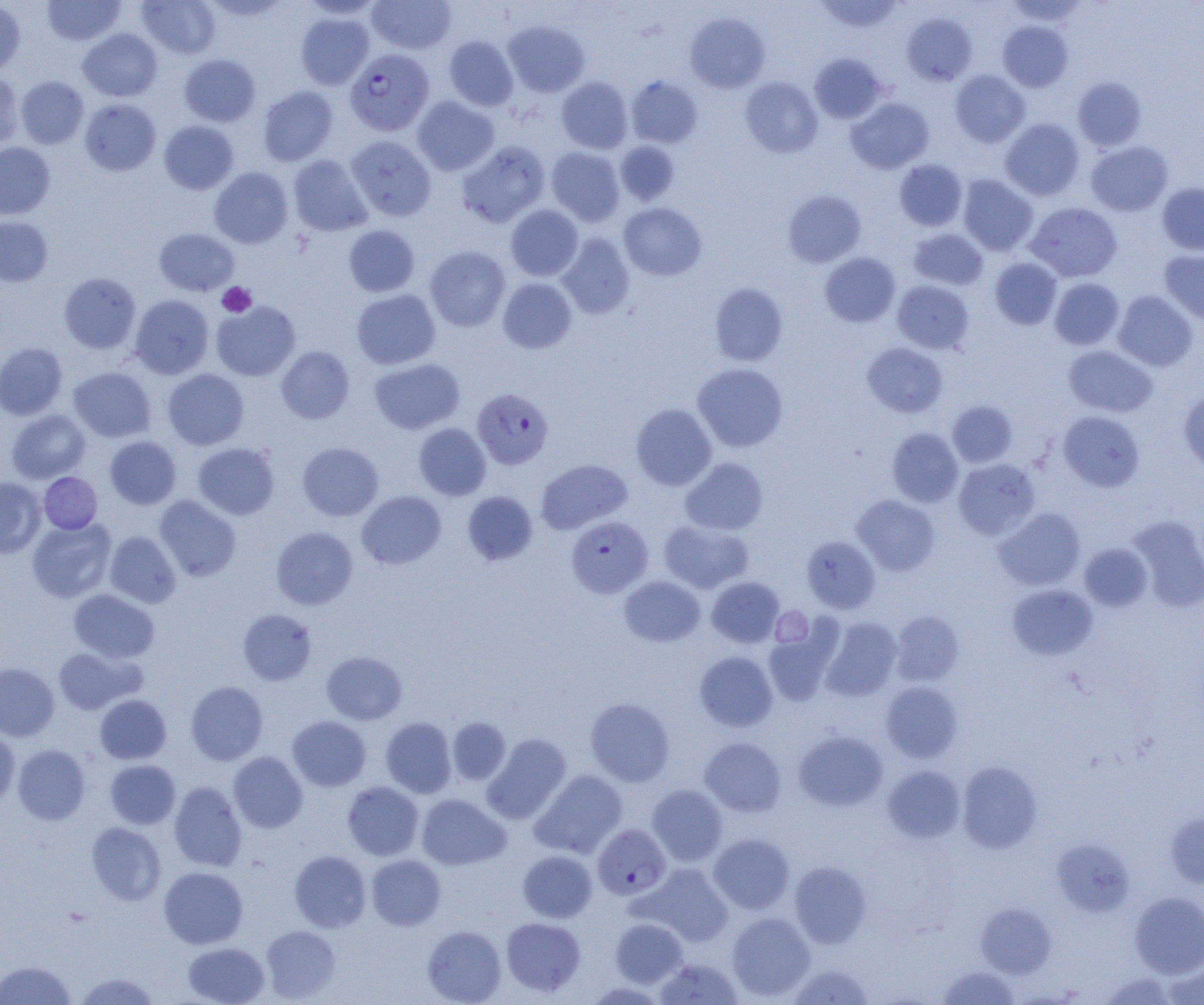
Approximate bounding boxes as [x1, y1, x2, y2] in pixels. Uninfected red blood cell locations: [42, 0, 126, 46], [137, 0, 220, 59], [367, 0, 456, 54], [814, 0, 905, 34], [0, 1, 26, 76], [299, 1, 384, 19], [1004, 1, 1088, 27], [295, 12, 374, 89], [685, 13, 770, 93], [902, 13, 977, 86], [503, 21, 589, 97], [998, 21, 1073, 91], [77, 29, 163, 101], [444, 35, 518, 111], [809, 53, 887, 124], [179, 54, 261, 126], [950, 70, 1030, 147], [0, 72, 23, 151], [626, 75, 703, 148], [16, 76, 89, 149], [556, 77, 633, 153], [740, 77, 823, 158], [1072, 77, 1147, 151], [257, 86, 338, 166], [412, 96, 499, 176], [846, 98, 934, 174], [79, 99, 161, 176], [1000, 118, 1084, 201], [159, 120, 239, 195], [346, 136, 436, 221], [456, 140, 550, 228], [615, 141, 680, 206], [1086, 141, 1174, 216], [0, 142, 55, 220], [546, 147, 625, 226], [288, 155, 372, 237], [894, 159, 967, 231], [209, 167, 293, 248], [958, 175, 1038, 256], [1156, 182, 1204, 255], [783, 189, 866, 268], [619, 202, 707, 280], [1025, 202, 1122, 282], [505, 205, 583, 281], [0, 216, 53, 286], [343, 225, 420, 297], [154, 228, 239, 295], [908, 228, 988, 291], [556, 233, 635, 319], [424, 246, 510, 332], [1160, 249, 1204, 323], [820, 252, 900, 327], [989, 257, 1063, 330], [58, 273, 141, 354], [1049, 277, 1124, 350], [498, 278, 577, 354], [892, 280, 974, 354], [709, 283, 788, 366], [351, 289, 440, 369], [1113, 291, 1198, 371], [129, 295, 214, 379], [211, 301, 301, 381], [0, 342, 67, 420], [862, 343, 948, 417], [1063, 345, 1158, 417], [276, 346, 355, 424], [369, 357, 465, 434], [692, 363, 788, 452], [68, 366, 156, 442], [162, 369, 248, 450], [1179, 388, 1204, 473], [947, 400, 1018, 467], [631, 403, 717, 491], [6, 409, 90, 483], [1058, 411, 1144, 491], [414, 423, 491, 500], [887, 427, 963, 507], [105, 436, 181, 509], [192, 442, 279, 520], [297, 442, 383, 521], [680, 457, 768, 536], [953, 458, 1040, 540], [536, 459, 632, 534], [39, 472, 102, 534], [0, 478, 46, 558], [357, 490, 447, 570], [462, 490, 538, 566], [155, 495, 241, 581], [851, 495, 940, 576], [993, 508, 1085, 591], [1127, 516, 1204, 612], [27, 517, 116, 603], [658, 519, 754, 593], [271, 527, 357, 609], [104, 531, 181, 608], [802, 535, 880, 614], [1080, 543, 1153, 611], [619, 576, 705, 647], [706, 577, 784, 648], [1007, 584, 1098, 660], [68, 589, 159, 663], [237, 609, 317, 685], [890, 611, 965, 686], [820, 617, 902, 701], [763, 622, 843, 707], [52, 646, 143, 714], [322, 651, 407, 725], [694, 651, 778, 732], [0, 663, 59, 741], [185, 681, 268, 765], [880, 681, 962, 762], [94, 694, 171, 764], [585, 697, 675, 786], [287, 715, 371, 791], [380, 717, 457, 798], [447, 717, 511, 785], [0, 727, 19, 807], [793, 731, 888, 811], [482, 733, 572, 825], [699, 737, 786, 816], [13, 744, 90, 825], [228, 752, 308, 833], [105, 760, 180, 829], [957, 761, 1042, 853], [883, 765, 965, 843], [530, 769, 627, 859], [169, 781, 247, 871], [342, 782, 423, 860], [647, 784, 727, 866], [416, 794, 510, 870], [1165, 811, 1204, 889], [85, 822, 166, 905], [708, 833, 795, 914], [1052, 839, 1135, 916], [289, 850, 371, 932], [517, 850, 597, 923], [366, 854, 446, 930], [788, 861, 872, 948], [636, 863, 733, 947], [159, 867, 248, 949], [1130, 891, 1204, 977], [976, 903, 1057, 978], [726, 912, 815, 1001], [501, 917, 585, 997], [610, 918, 687, 987], [261, 925, 340, 1002], [422, 925, 507, 1005], [183, 942, 269, 1005], [654, 958, 743, 1004], [1161, 959, 1204, 1005], [0, 960, 76, 1004], [786, 962, 875, 1005], [937, 966, 1019, 1004], [75, 973, 160, 1004], [1100, 973, 1176, 1004], [583, 982, 668, 1004]. Plasmodium falciparum-infected red blood cell locations: [344, 49, 435, 136], [472, 388, 554, 469], [566, 515, 653, 598], [592, 824, 671, 900]. Platelet locations: [217, 282, 257, 317], [771, 607, 813, 647]. Slide-level diagnosis: Plasmodium falciparum. Thin blood film. Image is 1204×1005 pixels. One field of a larger specimen. Optical microscopy. 1000x magnification.